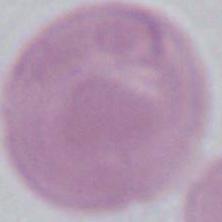

Summary:
  - Identification: red blood cell
  - Modality: micrograph
  - Magnification: 1000x